Outline platelets.
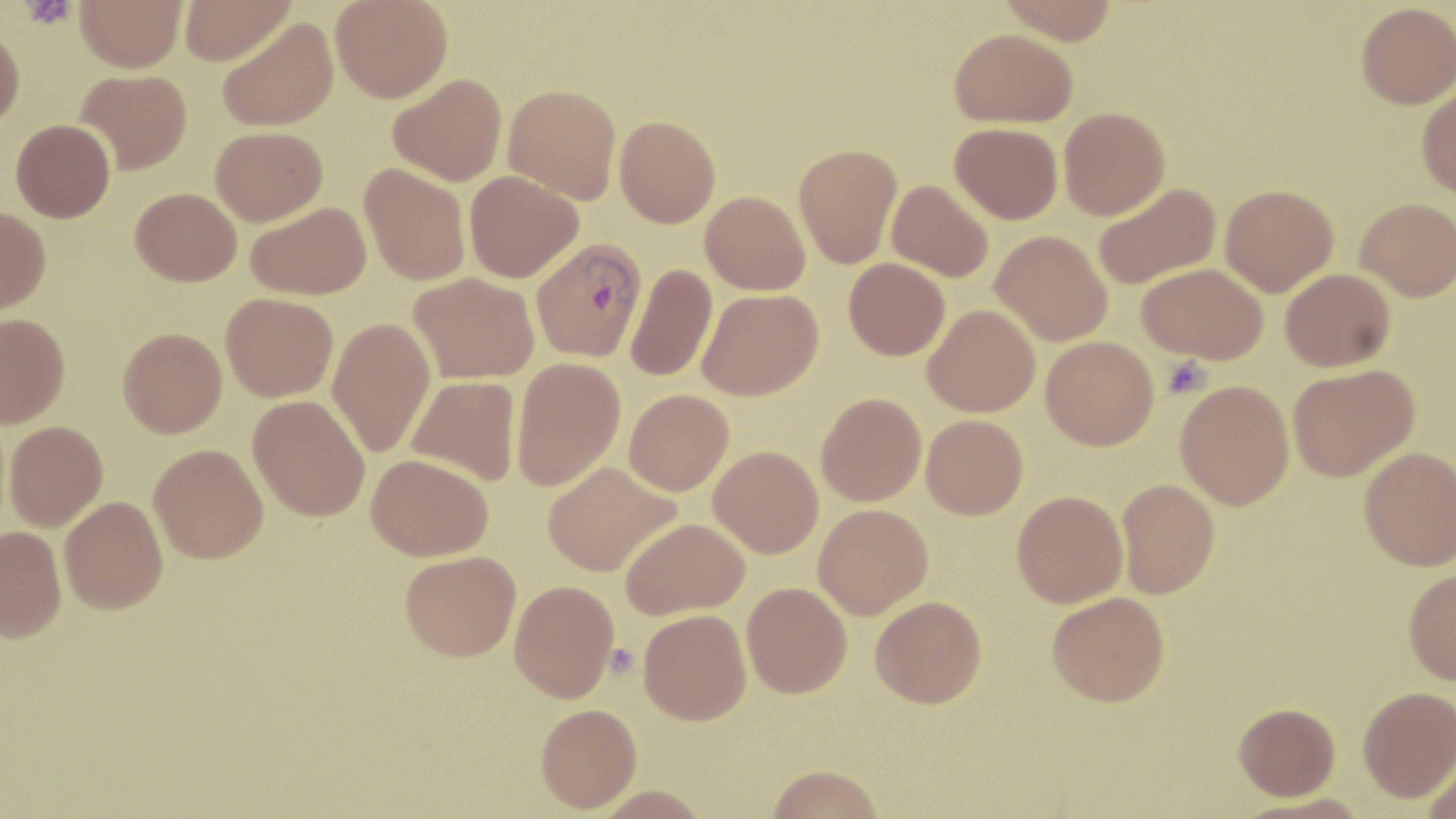

Approximate bounding boxes as (x1,y1)-(x2,y2) corner pairs in pixels.
Platelets: (21,0)-(76,30), (1162,356)-(1211,398).

Plasmodium vivax-infected red blood cell locations: (532,238)-(646,361). Uninfected red blood cell locations: (75,0)-(186,72), (179,0)-(294,64), (331,0)-(453,103), (996,0)-(1119,44), (1356,2)-(1456,108), (218,17)-(338,131), (0,25)-(25,130), (949,27)-(1077,127), (76,69)-(192,173), (388,73)-(507,186), (1417,83)-(1456,198), (503,84)-(621,203), (1059,107)-(1170,220), (615,115)-(721,227), (11,119)-(115,222), (950,123)-(1063,223), (210,126)-(327,225), (794,143)-(903,268), (359,162)-(471,285), (465,171)-(583,282), (886,179)-(994,282), (1093,182)-(1221,289), (1220,183)-(1339,296), (130,187)-(241,286), (701,190)-(810,294), (1356,197)-(1456,300), (246,201)-(371,300), (0,206)-(50,313), (991,230)-(1113,346), (844,258)-(950,360), (626,263)-(717,382), (1137,263)-(1268,364), (1280,268)-(1396,371), (409,272)-(539,383), (698,288)-(823,400), (221,292)-(338,401), (923,304)-(1041,417), (0,313)-(70,428), (327,317)-(436,456), (118,327)-(227,438), (1041,336)-(1159,449), (511,356)-(625,490), (1287,364)-(1419,481), (406,375)-(522,486), (1175,380)-(1294,510), (624,389)-(734,495), (816,392)-(927,506), (248,395)-(370,521), (921,414)-(1028,519), (4,420)-(107,531), (149,443)-(268,563), (709,445)-(823,557), (1359,447)-(1456,570), (366,454)-(493,560), (543,461)-(681,576), (1116,479)-(1220,598), (1012,490)-(1128,607), (59,497)-(168,614), (813,503)-(933,619), (621,517)-(749,618), (0,526)-(66,643), (400,550)-(521,661), (1403,567)-(1456,684), (509,579)-(620,702), (742,581)-(853,697), (1047,592)-(1170,706), (870,596)-(987,708), (639,609)-(752,725), (1357,686)-(1456,801), (1234,702)-(1341,800), (535,703)-(641,812), (1422,751)-(1456,819), (764,765)-(885,818). Slide-level diagnosis: Plasmodium vivax. Light microscopy. Thin blood film. Image is 1456×819 pixels. 1000x magnification. May-Grünwald-Giemsa-stained preparation. One field of a larger specimen.